Locate cells.
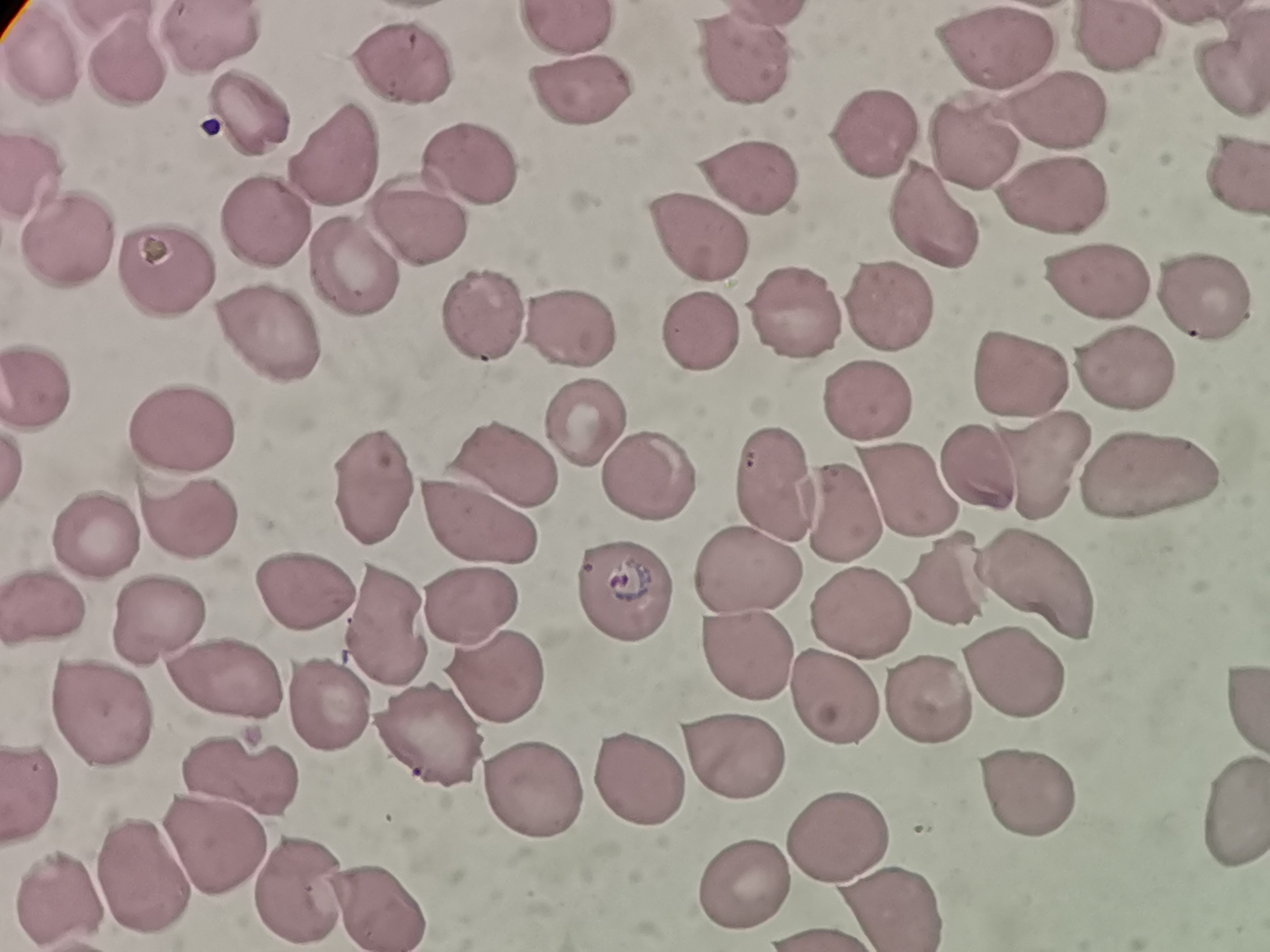
Approximate centers as {x, y} in pixels.
Cells: {562, 27}, {212, 36}, {1118, 43}, {990, 51}, {41, 58}, {743, 64}, {128, 67}, {395, 71}, {1227, 82}, {575, 93}, {251, 117}, {1055, 121}, {884, 143}, {975, 148}, {338, 157}, {456, 160}, {1233, 173}, {29, 179}, {752, 186}, {1060, 210}, {933, 216}, {269, 223}, {418, 228}, {703, 243}, {70, 245}, {170, 268}, {350, 270}, {1105, 290}, {1201, 302}, {473, 312}, {790, 315}, {892, 320}, {702, 326}, {579, 333}, {272, 336}, {1118, 371}, {1022, 374}, {35, 385}, {858, 403}, {587, 420}, {181, 431}, {502, 461}, {1044, 468}, {648, 476}, {371, 477}, {771, 482}, {1147, 484}, {905, 491}, {832, 510}, {482, 515}, {179, 521}, {99, 542}, {750, 565}, {1035, 573}, {311, 587}, {612, 588}, {958, 588}, {469, 595}, {43, 603}, {849, 611}, {152, 619}, {391, 622}, {749, 647}, {1010, 677}, {229, 679}, {497, 680}, {830, 691}, {1241, 697}, {926, 706}, {333, 709}, {94, 710}, {431, 733}, {728, 757}, {241, 777}, {633, 785}, {1030, 787}, {35, 789}, {517, 795}, {1232, 810}, {839, 837}, {215, 845}, {141, 861}, {296, 886}, {751, 888}, {373, 894}, {63, 897}, {887, 904}.

preparation = thin blood film
field of view = single
stain = Giemsa
capture = smartphone through the microscope eyepiece
image size = 1270×952 pixels